Locate every blood parasite and identify its species.
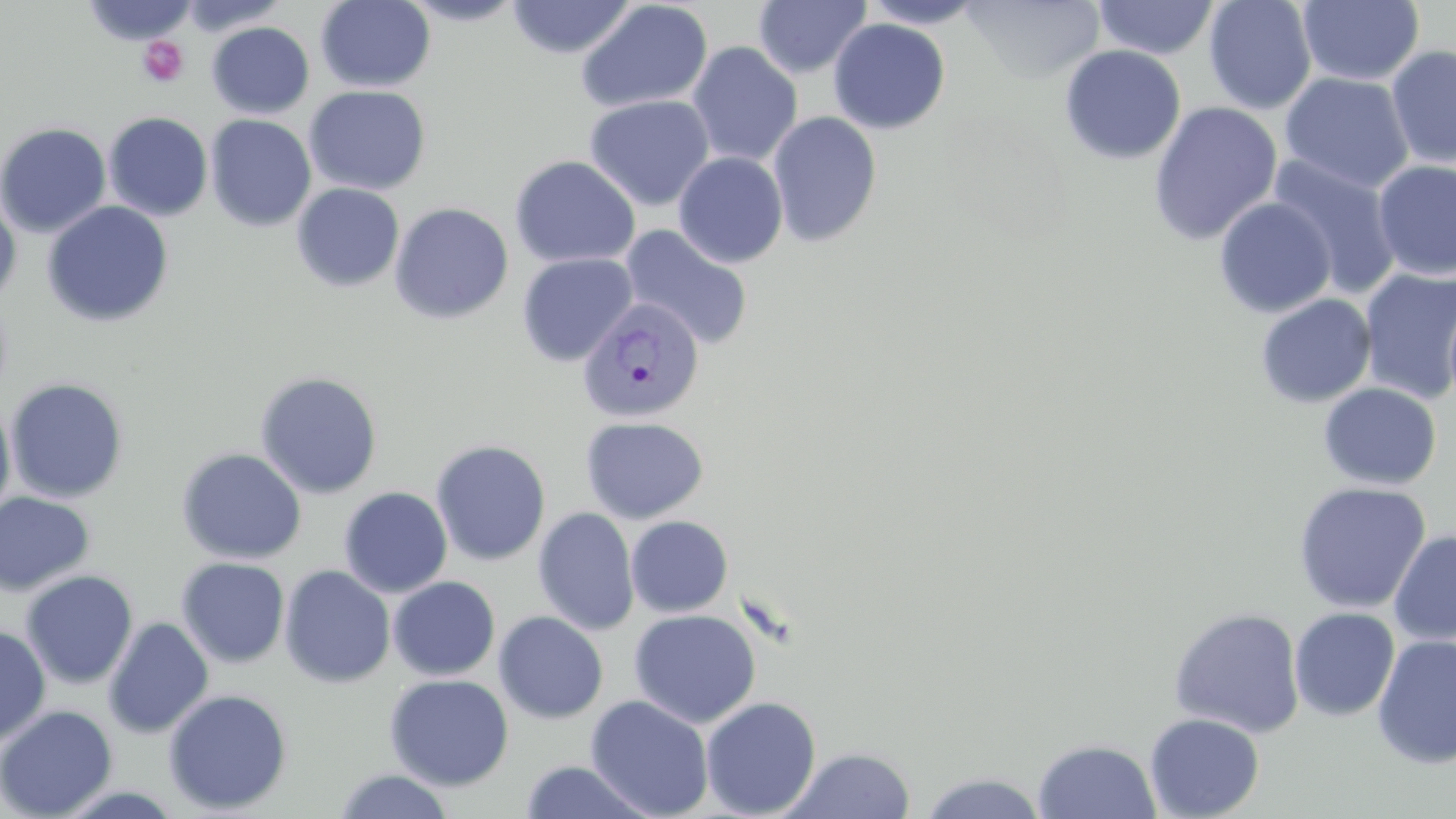

Approximate bounding boxes as (x1, y1, x2, y2) in pixels.
Plasmodium vivax-infected red blood cells: (577, 297, 705, 424).
No Plasmodium falciparum, Plasmodium ovale, Plasmodium malariae, Babesia divergens, or Trypanosoma brucei observed.

Uninfected red blood cell locations: (84, 0, 200, 45), (399, 0, 529, 26), (506, 0, 636, 59), (753, 0, 872, 79), (860, 0, 989, 28), (961, 0, 1105, 84), (1092, 0, 1221, 60), (1203, 0, 1317, 115), (1297, 0, 1424, 87), (315, 1, 436, 92), (575, 1, 714, 113), (828, 18, 950, 134), (206, 22, 314, 119), (686, 41, 803, 167), (1059, 44, 1186, 165), (1386, 44, 1456, 168), (1280, 72, 1415, 194), (304, 85, 431, 195), (584, 95, 716, 211), (1148, 101, 1283, 246), (767, 111, 882, 248), (103, 112, 213, 221), (205, 115, 316, 232), (0, 122, 111, 238), (673, 152, 789, 267), (509, 155, 641, 268), (1267, 155, 1404, 299), (1372, 159, 1456, 280), (292, 183, 405, 292), (0, 194, 22, 306), (1213, 197, 1337, 318), (42, 200, 174, 328), (389, 202, 514, 324), (618, 224, 754, 351), (516, 252, 638, 367), (1359, 267, 1456, 404), (1255, 294, 1377, 409), (255, 371, 383, 499), (4, 378, 129, 503), (1318, 382, 1442, 489), (0, 397, 16, 527), (580, 416, 709, 524), (430, 439, 551, 566), (176, 448, 306, 564), (1293, 481, 1431, 614), (338, 487, 453, 598), (0, 491, 96, 596), (533, 507, 639, 635), (625, 515, 733, 618), (1388, 530, 1456, 646), (176, 557, 290, 668), (279, 565, 396, 688), (20, 570, 139, 690), (388, 576, 500, 681), (1168, 606, 1305, 738), (1289, 607, 1400, 721), (628, 609, 761, 728), (494, 611, 609, 723), (103, 616, 214, 738), (0, 625, 51, 748), (1372, 635, 1456, 769), (384, 674, 514, 791), (163, 688, 293, 815), (585, 695, 715, 819), (700, 696, 822, 818), (0, 705, 118, 818), (1144, 713, 1265, 819), (1033, 738, 1162, 818), (784, 747, 916, 818), (517, 759, 659, 818), (331, 769, 456, 819), (916, 771, 1051, 818). Platelet locations: (138, 37, 190, 87). Slide-level diagnosis: Plasmodium vivax. Light microscopy. May-Grünwald-Giemsa stain. Captured at 1000x magnification. One field of a larger specimen. Image is 1456×819 pixels. Thin blood film.